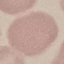

Summary:
  - Result: negative for malaria parasites
  - Preparation: thin blood smear
  - Capture: smartphone camera at the microscope eyepiece
  - Image type: cell patch, automatically extracted from a larger field of view and resized to 64 × 64 pixels
  - Stain: Giemsa